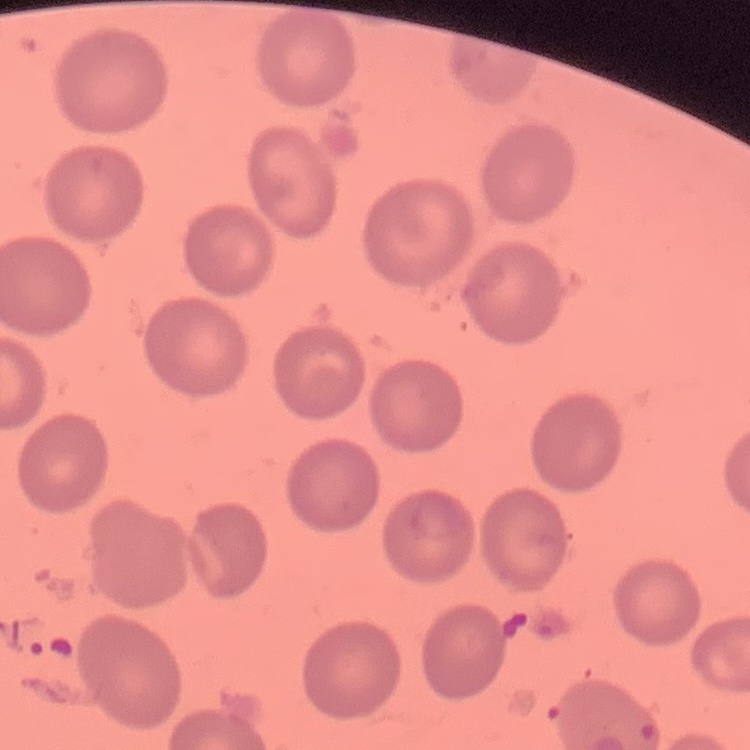

red blood cell morphology = no rouleaux formation
preparation = thin peripheral smear
stain = Field's or Giemsa
image type = one tile cut from a larger photomicrograph